Assess this cell for malaria.
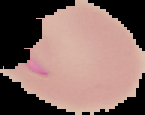
Parasitized.

Image is 145×115 pixels. From a thin blood smear. Cell region segmented out of the field of view; the surrounding area is masked to black.